Give the extent of all uninfected red blood cells.
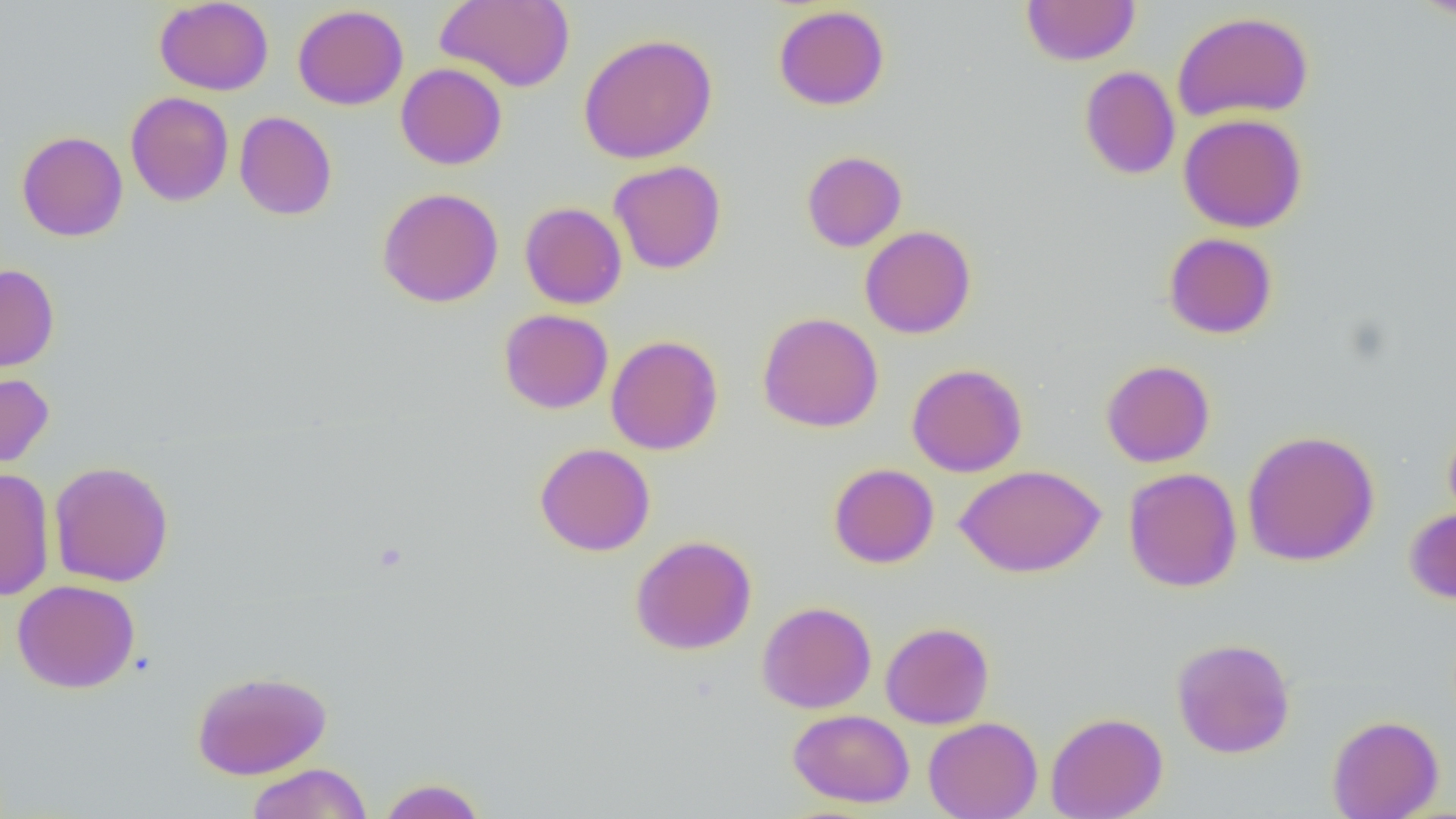
Approximate bounding boxes as named x1/y1/x2/y2 corners in pixels.
Uninfected red blood cells: (x1=154, y1=0, x2=274, y2=95), (x1=436, y1=0, x2=575, y2=92), (x1=1021, y1=0, x2=1140, y2=66), (x1=1411, y1=0, x2=1456, y2=19), (x1=292, y1=4, x2=409, y2=110), (x1=773, y1=5, x2=890, y2=111), (x1=1171, y1=11, x2=1314, y2=123), (x1=578, y1=33, x2=718, y2=164), (x1=396, y1=63, x2=507, y2=170), (x1=1079, y1=65, x2=1180, y2=180), (x1=125, y1=91, x2=234, y2=206), (x1=234, y1=111, x2=337, y2=220), (x1=1178, y1=113, x2=1307, y2=233), (x1=16, y1=130, x2=128, y2=242), (x1=801, y1=150, x2=907, y2=252), (x1=608, y1=160, x2=727, y2=274), (x1=376, y1=187, x2=504, y2=307), (x1=519, y1=202, x2=628, y2=309), (x1=859, y1=225, x2=976, y2=339), (x1=1163, y1=232, x2=1278, y2=339), (x1=0, y1=264, x2=59, y2=374), (x1=498, y1=309, x2=613, y2=414), (x1=757, y1=312, x2=884, y2=433), (x1=606, y1=334, x2=723, y2=455), (x1=1100, y1=359, x2=1215, y2=468), (x1=906, y1=362, x2=1028, y2=477), (x1=0, y1=372, x2=54, y2=471), (x1=1443, y1=420, x2=1456, y2=530), (x1=1242, y1=430, x2=1380, y2=567), (x1=534, y1=442, x2=655, y2=556), (x1=49, y1=460, x2=174, y2=587), (x1=828, y1=463, x2=939, y2=568), (x1=955, y1=464, x2=1105, y2=577), (x1=0, y1=467, x2=55, y2=601), (x1=1123, y1=467, x2=1243, y2=592), (x1=1404, y1=505, x2=1456, y2=605), (x1=629, y1=535, x2=758, y2=655), (x1=11, y1=578, x2=141, y2=694), (x1=757, y1=600, x2=876, y2=714), (x1=880, y1=621, x2=994, y2=729), (x1=1171, y1=637, x2=1296, y2=759), (x1=191, y1=670, x2=332, y2=780), (x1=787, y1=709, x2=915, y2=808), (x1=1045, y1=711, x2=1168, y2=819), (x1=1327, y1=714, x2=1444, y2=819), (x1=923, y1=716, x2=1043, y2=819), (x1=246, y1=763, x2=373, y2=818), (x1=377, y1=777, x2=488, y2=819).

slide-level diagnosis = negative for blood parasites
magnification = 1000x
preparation = thin blood smear
field of view = single
modality = optical microscopy
image size = 1456×819 pixels